Report the malaria status of this cell.
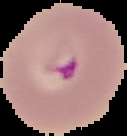

It is parasitized.

The area outside the segmented cell region is set to black. From a thin blood smear. Image is 127×136 pixels.